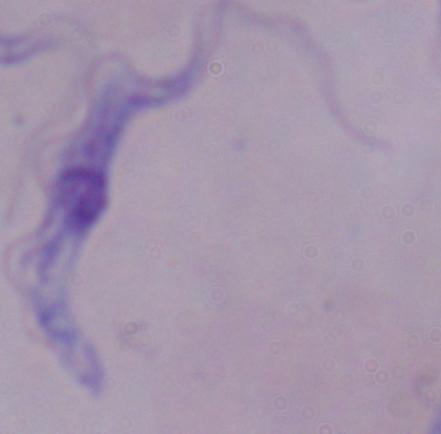
{
  "identification": "trypanosome",
  "magnification": "1000x",
  "modality": "photomicrograph"
}